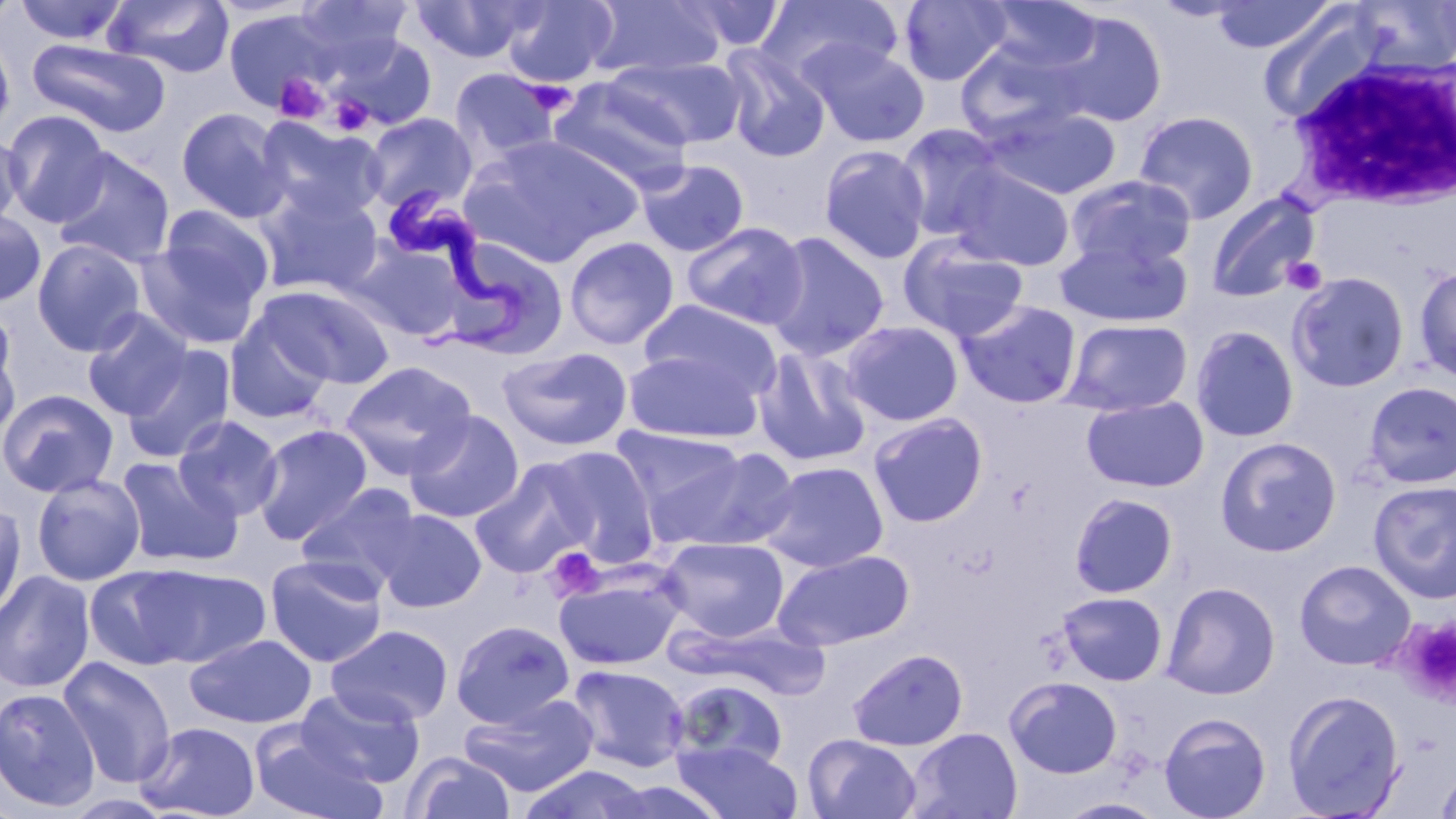 Approximate bounding boxes as (x1, y1, x2, y2) in pixels. Trypanosoma brucei locations: (389, 185, 531, 348). Platelet locations: (272, 73, 332, 124), (524, 80, 578, 115), (329, 94, 373, 135), (1282, 256, 1328, 295), (546, 547, 606, 601), (1396, 617, 1456, 704). White blood cell locations: (1289, 49, 1456, 212). Uninfected red blood cell locations: (0, 0, 24, 27), (13, 0, 130, 45), (104, 0, 234, 78), (293, 0, 414, 67), (501, 0, 618, 88), (587, 0, 727, 80), (753, 0, 904, 89), (897, 0, 1014, 86), (979, 0, 1104, 76), (411, 1, 540, 64), (674, 1, 787, 54), (1209, 1, 1337, 54), (1351, 1, 1456, 74), (1258, 6, 1385, 122), (222, 8, 336, 116), (1044, 8, 1169, 128), (0, 29, 15, 140), (332, 34, 437, 130), (26, 38, 171, 138), (954, 41, 1084, 145), (801, 42, 931, 148), (719, 44, 832, 163), (605, 55, 746, 150), (451, 68, 562, 161), (548, 80, 695, 186), (983, 104, 1122, 202), (176, 107, 291, 223), (1133, 110, 1259, 224), (3, 111, 112, 227), (363, 112, 478, 213), (255, 117, 388, 224), (895, 124, 1009, 242), (0, 131, 26, 231), (460, 134, 645, 268), (819, 145, 930, 265), (51, 148, 176, 269), (636, 159, 750, 258), (946, 163, 1076, 271), (1065, 175, 1198, 272), (256, 186, 383, 296), (1205, 192, 1321, 303), (144, 203, 275, 329), (0, 208, 46, 309), (681, 221, 809, 331), (764, 232, 890, 361), (899, 234, 1029, 341), (1054, 235, 1192, 329), (564, 236, 679, 350), (442, 237, 570, 361), (32, 239, 147, 357), (349, 240, 470, 341), (1414, 264, 1456, 382), (1286, 272, 1410, 393), (265, 286, 395, 389), (638, 299, 782, 400), (955, 299, 1082, 409), (82, 309, 193, 420), (224, 317, 334, 425), (1063, 318, 1193, 416), (839, 320, 965, 427), (0, 322, 20, 449), (1190, 325, 1300, 443), (120, 346, 236, 464), (497, 346, 633, 451), (752, 346, 872, 468), (623, 348, 764, 444), (341, 361, 477, 479), (1363, 382, 1456, 488), (0, 389, 118, 498), (1081, 395, 1209, 493), (404, 409, 525, 524), (868, 412, 988, 527), (172, 415, 285, 522), (252, 424, 373, 546), (610, 426, 746, 521), (1215, 437, 1342, 557), (545, 446, 660, 566), (655, 446, 801, 553), (116, 456, 242, 569), (469, 460, 596, 579), (758, 461, 889, 572), (31, 473, 145, 585), (1368, 480, 1456, 603), (294, 483, 423, 594), (1069, 492, 1179, 598), (0, 502, 26, 623), (374, 508, 486, 613), (657, 536, 790, 641), (772, 549, 915, 650), (264, 554, 389, 668), (1294, 559, 1416, 670), (85, 565, 202, 670), (136, 565, 270, 667), (554, 568, 684, 671), (0, 570, 96, 693), (1161, 581, 1281, 700), (1056, 591, 1169, 686), (451, 619, 575, 729), (326, 624, 453, 727), (184, 633, 317, 728), (847, 648, 968, 751), (57, 656, 177, 789), (566, 664, 690, 773), (1004, 675, 1123, 779), (670, 678, 789, 774), (296, 686, 425, 788), (0, 687, 102, 813), (1282, 689, 1405, 818), (457, 693, 600, 798), (1158, 711, 1271, 819), (136, 721, 261, 819), (906, 727, 1024, 819), (250, 728, 388, 819), (803, 733, 922, 818), (673, 740, 802, 818), (402, 752, 516, 819), (1433, 761, 1456, 819), (519, 765, 657, 819). Slide-level diagnosis: Trypanosoma brucei. Light microscopy. Single field of view. 1000x magnification. Thin blood smear. Image is 1456×819 pixels. May-Grünwald-Giemsa-stained preparation.